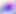

Summary:
  - Magnification: 400x
  - Identification: Toxoplasma gondii
  - Modality: photomicrograph